Comment on the morphology of the erythrocytes.
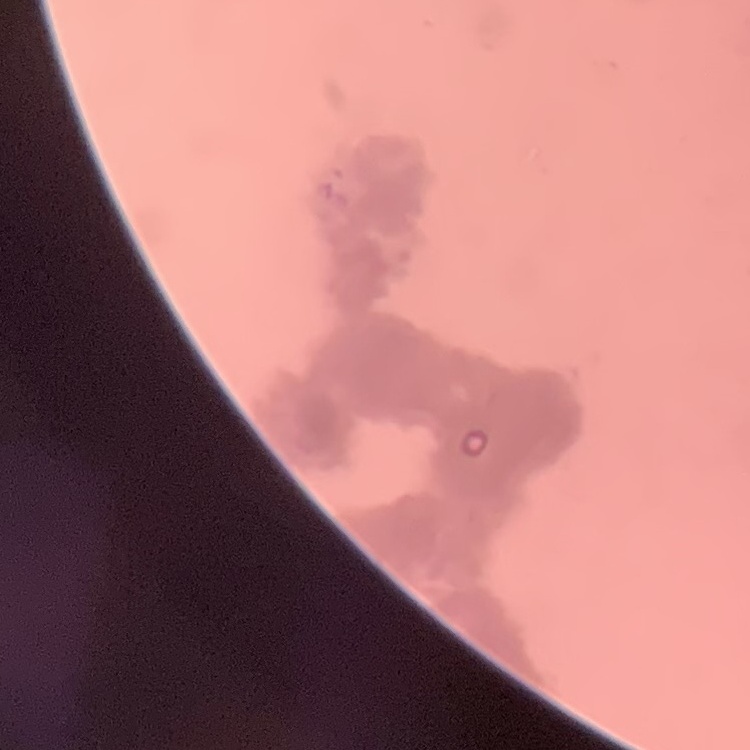

Rouleaux formation.

One tile cut from a larger photomicrograph. Field's or Giemsa stain. Thin blood smear.